Locate and identify every blood parasite.
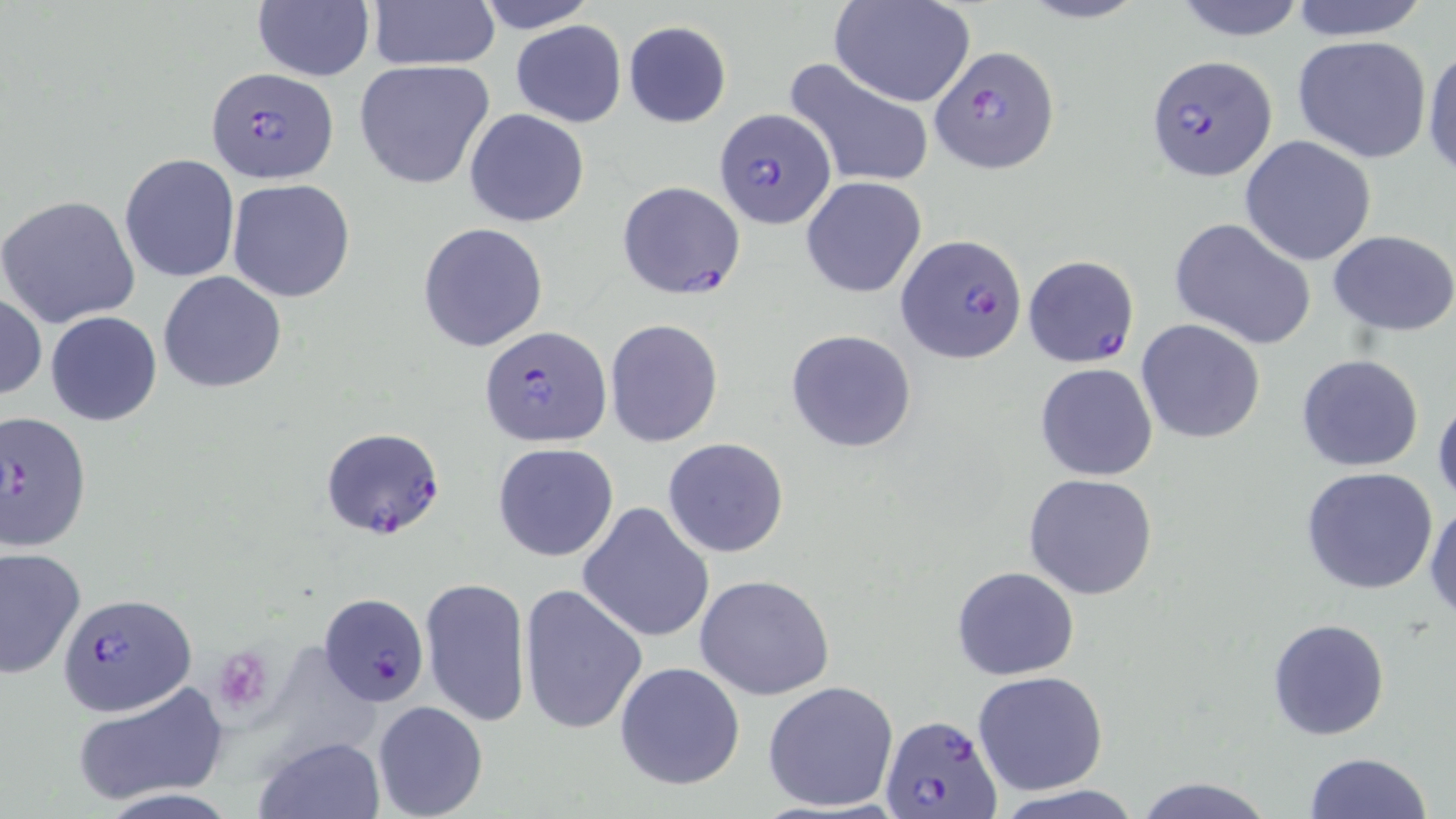

Approximate bounding boxes as [x1, y1, x2, y2] in pixels.
Plasmodium falciparum-infected red blood cells: [931, 45, 1062, 173], [1147, 55, 1279, 183], [205, 67, 337, 183], [713, 107, 836, 230], [617, 180, 746, 301], [897, 233, 1028, 362], [1024, 254, 1139, 370], [480, 323, 612, 449], [1, 412, 94, 551], [321, 427, 445, 539], [58, 592, 197, 715], [318, 593, 427, 704], [880, 714, 1003, 819].
No Plasmodium ovale, Plasmodium malariae, Plasmodium vivax, Babesia divergens, or Trypanosoma brucei observed.

Summary:
  - Uninfected red blood cell locations: [365, 0, 499, 70], [477, 0, 596, 33], [830, 0, 976, 107], [1016, 0, 1152, 25], [1170, 0, 1310, 42], [1285, 0, 1433, 41], [251, 2, 374, 82], [510, 19, 627, 127], [622, 20, 732, 128], [1291, 36, 1432, 163], [1423, 45, 1456, 182], [784, 56, 934, 190], [353, 59, 495, 191], [465, 108, 589, 228], [1240, 136, 1379, 266], [118, 152, 240, 284], [801, 177, 927, 298], [227, 179, 355, 303], [0, 194, 140, 327], [1170, 217, 1316, 350], [418, 223, 548, 351], [1328, 230, 1456, 333], [158, 270, 287, 393], [0, 292, 46, 400], [45, 310, 162, 427], [604, 319, 724, 447], [1136, 319, 1266, 444], [784, 329, 918, 454], [1296, 353, 1424, 472], [1034, 363, 1158, 482], [1432, 392, 1456, 514], [662, 438, 789, 558], [492, 443, 619, 562], [1301, 466, 1439, 594], [1023, 474, 1159, 599], [1425, 499, 1456, 621], [577, 502, 715, 642], [0, 547, 87, 680], [951, 566, 1079, 681], [695, 574, 838, 701], [420, 575, 531, 728], [519, 582, 649, 734], [1267, 617, 1392, 740], [614, 662, 747, 791], [971, 670, 1109, 796], [762, 679, 900, 814], [70, 681, 229, 806], [372, 700, 489, 819], [252, 734, 387, 818], [1304, 751, 1435, 819], [1130, 774, 1279, 819], [992, 787, 1146, 819]
  - Platelet locations: [225, 654, 267, 706]
  - Slide-level diagnosis: Plasmodium falciparum
  - Field of view: single
  - Image size: 1456×819 pixels
  - Modality: optical microscopy
  - Preparation: thin blood film
  - Magnification: 1000x
  - Stain: May-Grünwald-Giemsa